Identify the blood parasite species.
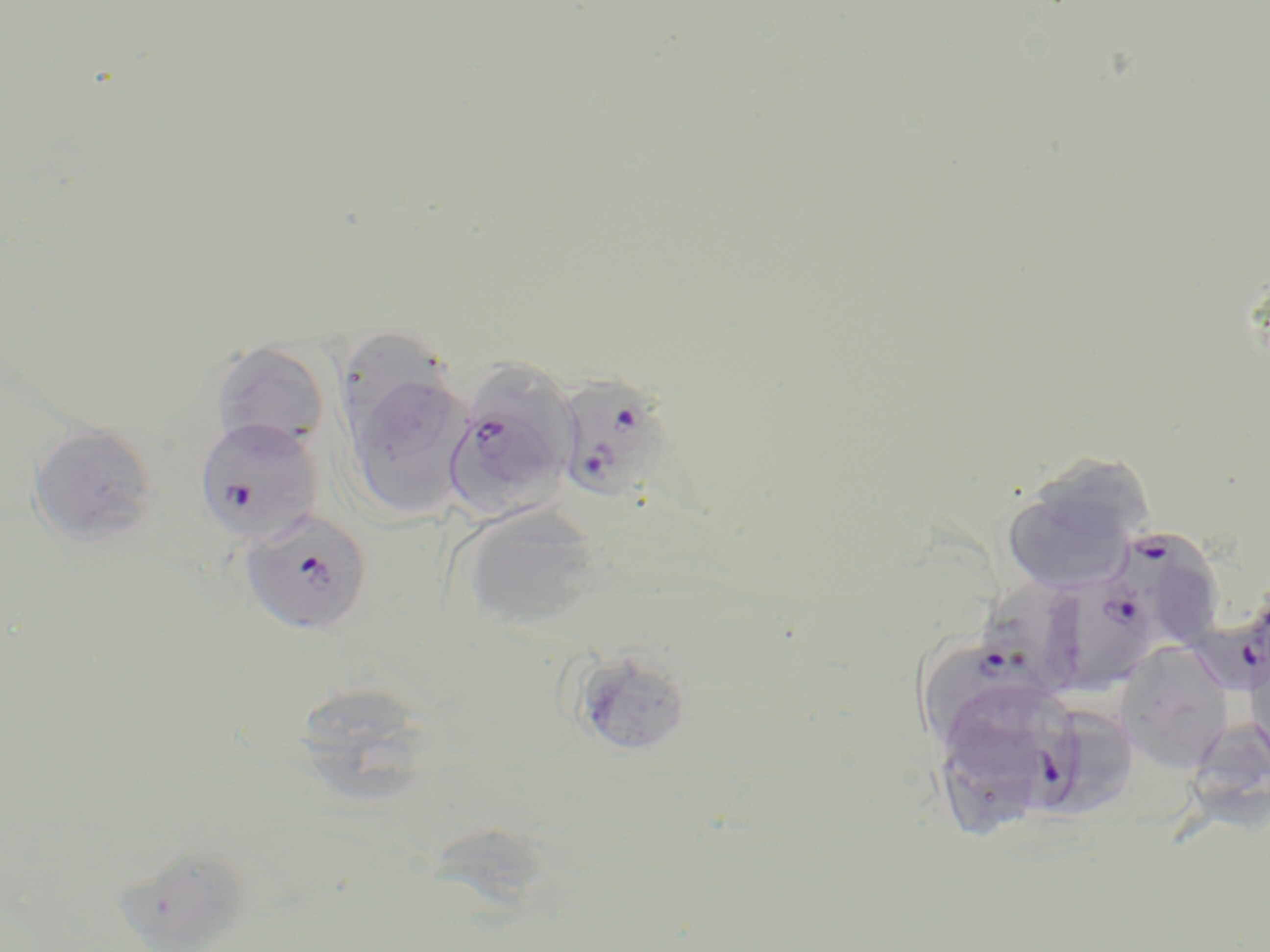

Plasmodium falciparum.

{
  "uninfected_red_blood_cell_locations": "approximate bounding boxes as (x1, y1, x2, y2) in pixels: (346, 326, 445, 439), (211, 340, 331, 452), (480, 358, 581, 461), (358, 382, 472, 519), (28, 424, 159, 547), (999, 466, 1147, 597), (458, 507, 605, 635), (1114, 640, 1235, 772), (1245, 645, 1270, 771), (569, 647, 693, 757), (306, 690, 422, 813), (1060, 706, 1140, 820), (1189, 721, 1270, 834), (117, 849, 253, 952)",
  "magnification": "1000x",
  "stain": "May-Grünwald-Giemsa",
  "modality": "light microscopy",
  "plasmodium_falciparum_infected_red_blood_cell_locations": "approximate bounding boxes as (x1, y1, x2, y2) in pixels: (563, 375, 679, 505), (447, 406, 559, 514), (194, 416, 323, 545), (239, 509, 374, 636), (1127, 532, 1223, 653), (1043, 569, 1162, 695), (1195, 612, 1270, 689), (926, 643, 1057, 746), (928, 678, 1088, 831)",
  "preparation": "thin blood smear",
  "field_of_view": "single",
  "image_size": "1270×952 pixels"
}